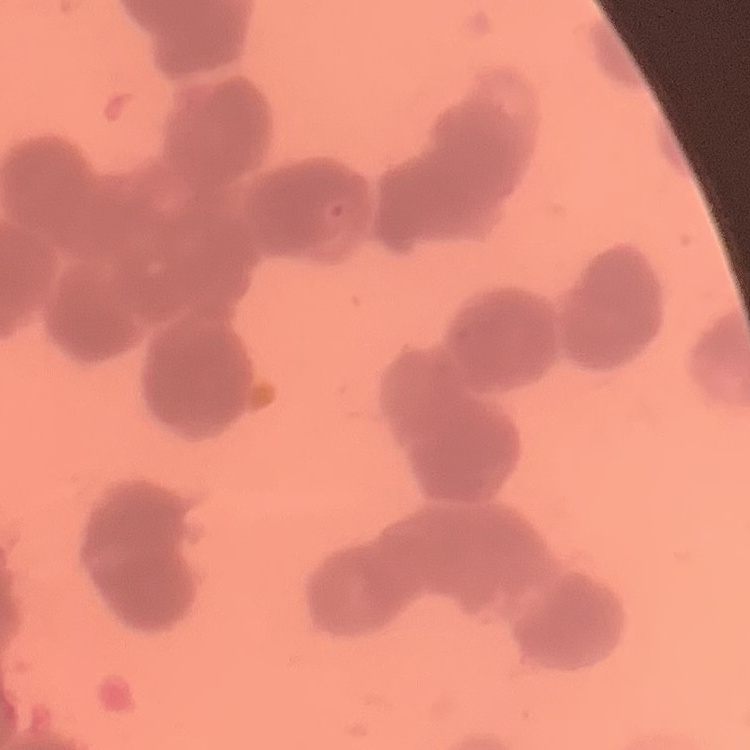
red blood cell morphology = rouleaux formation
preparation = thin blood smear
image type = square crop of a larger photomicrograph
stain = Field's or Giemsa